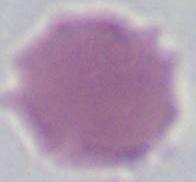

Photomicrograph. Captured at 1000x magnification. A red blood cell is seen.